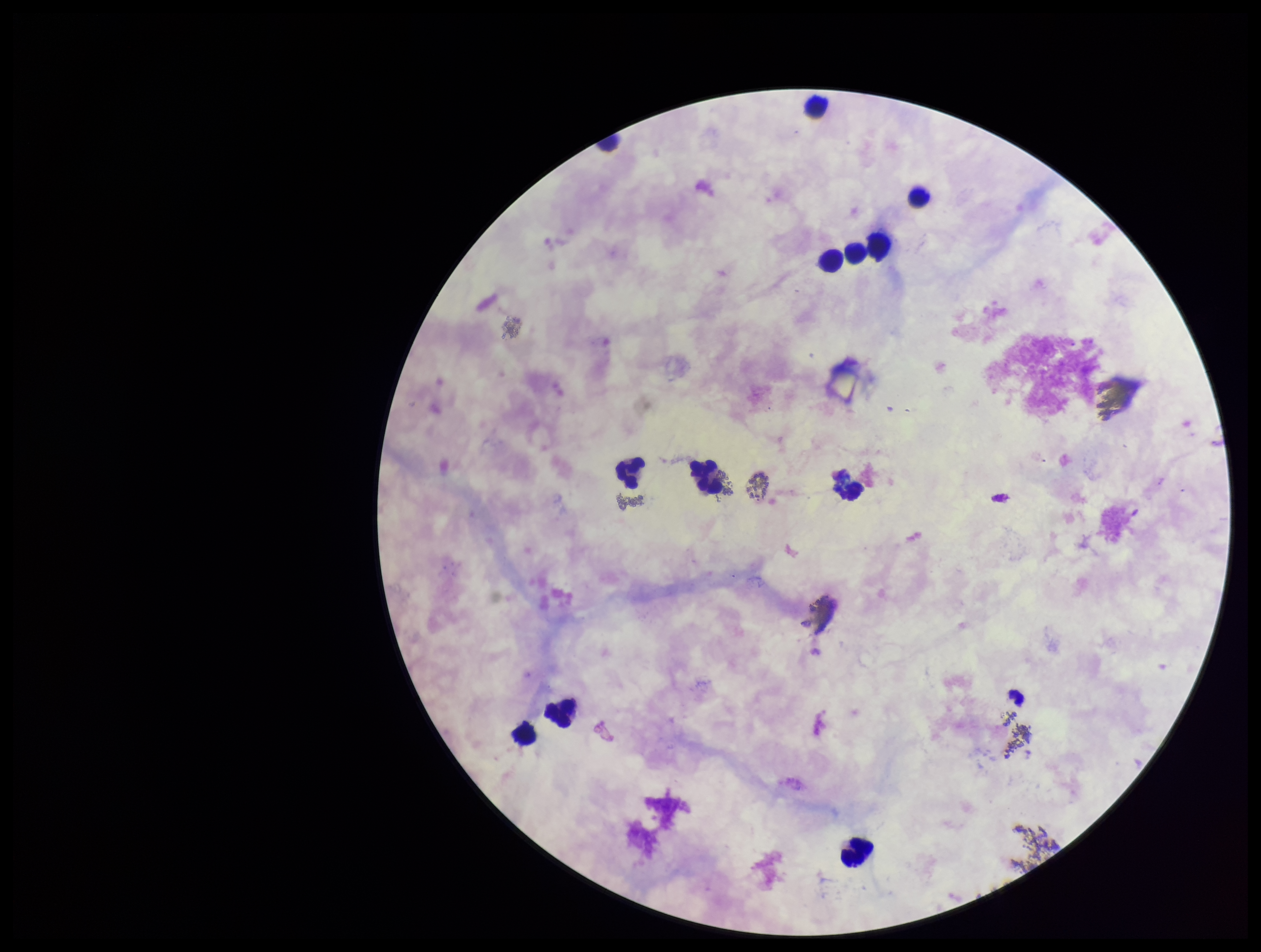

Plasmodium parasites = none identified
image size = 1261×952 pixels
capture = smartphone photograph through the microscope eyepiece
parasite count = 0
patient malaria status = negative
field of view = single
leukocyte count = 12
preparation = thick smear
stain = Giemsa